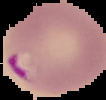

image type = segmented cell region on a black background
preparation = thin blood film
result = malaria parasites detected
image size = 106×100 pixels